Outline platelets.
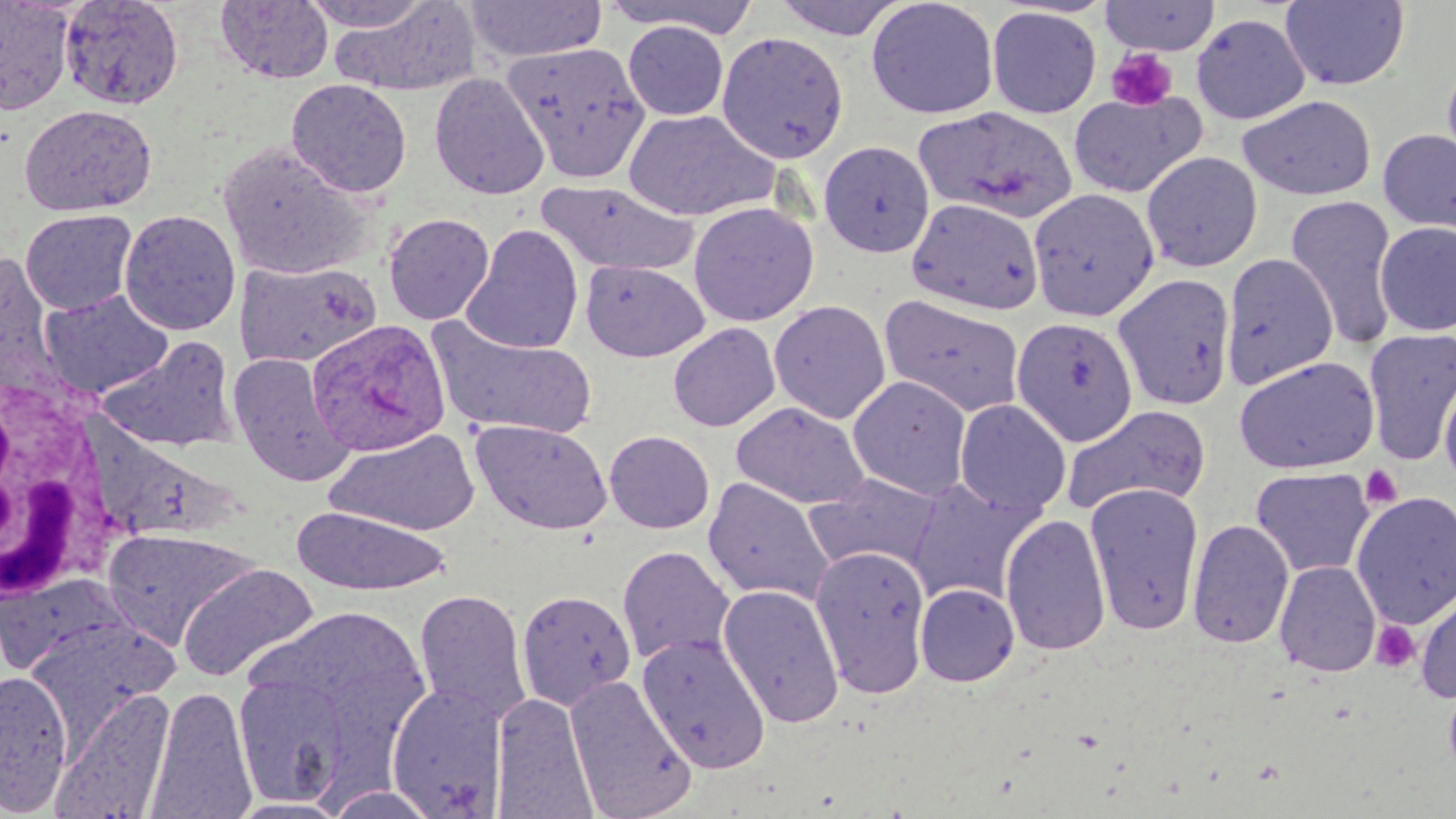
Approximate bounding boxes as named x1/y1/x2/y2 corners in pixels.
Platelets: (x1=1106, y1=48, x2=1179, y2=112), (x1=1360, y1=465, x2=1403, y2=508), (x1=1370, y1=620, x2=1420, y2=672).

Summary:
  - Plasmodium ovale-infected red blood cell locations: (x1=306, y1=319, x2=451, y2=456)
  - White blood cell locations: (x1=0, y1=368, x2=113, y2=607)
  - Uninfected red blood cell locations: (x1=0, y1=0, x2=75, y2=115), (x1=59, y1=0, x2=184, y2=110), (x1=300, y1=0, x2=435, y2=31), (x1=465, y1=0, x2=607, y2=63), (x1=771, y1=0, x2=911, y2=41), (x1=865, y1=0, x2=999, y2=119), (x1=215, y1=1, x2=334, y2=85), (x1=599, y1=1, x2=762, y2=38), (x1=1098, y1=1, x2=1222, y2=55), (x1=1279, y1=1, x2=1409, y2=90), (x1=332, y1=2, x2=480, y2=97), (x1=986, y1=6, x2=1102, y2=119), (x1=1191, y1=14, x2=1310, y2=124), (x1=623, y1=20, x2=729, y2=121), (x1=716, y1=30, x2=849, y2=164), (x1=504, y1=41, x2=650, y2=180), (x1=1440, y1=59, x2=1456, y2=184), (x1=429, y1=72, x2=550, y2=200), (x1=286, y1=78, x2=412, y2=197), (x1=1068, y1=90, x2=1207, y2=199), (x1=1237, y1=95, x2=1376, y2=201), (x1=19, y1=104, x2=157, y2=216), (x1=915, y1=105, x2=1078, y2=224), (x1=624, y1=109, x2=779, y2=222), (x1=1378, y1=127, x2=1456, y2=236), (x1=818, y1=140, x2=935, y2=257), (x1=217, y1=142, x2=373, y2=280), (x1=1141, y1=151, x2=1263, y2=272), (x1=538, y1=179, x2=696, y2=277), (x1=1028, y1=188, x2=1159, y2=321), (x1=1285, y1=195, x2=1399, y2=351), (x1=906, y1=197, x2=1044, y2=315), (x1=688, y1=202, x2=819, y2=326), (x1=20, y1=208, x2=138, y2=314), (x1=119, y1=209, x2=241, y2=335), (x1=383, y1=212, x2=495, y2=325), (x1=1374, y1=222, x2=1456, y2=337), (x1=461, y1=224, x2=584, y2=355), (x1=1220, y1=253, x2=1338, y2=390), (x1=0, y1=254, x2=59, y2=388), (x1=235, y1=259, x2=382, y2=368), (x1=581, y1=260, x2=710, y2=362), (x1=1112, y1=273, x2=1237, y2=410), (x1=39, y1=289, x2=174, y2=398), (x1=879, y1=294, x2=1026, y2=418), (x1=769, y1=299, x2=891, y2=424), (x1=428, y1=317, x2=597, y2=440), (x1=1011, y1=317, x2=1139, y2=446), (x1=667, y1=322, x2=781, y2=432), (x1=1363, y1=328, x2=1456, y2=465), (x1=96, y1=336, x2=240, y2=452), (x1=228, y1=353, x2=354, y2=486), (x1=1233, y1=355, x2=1380, y2=474), (x1=1439, y1=371, x2=1456, y2=493), (x1=848, y1=375, x2=972, y2=499), (x1=954, y1=399, x2=1071, y2=517), (x1=731, y1=402, x2=870, y2=510), (x1=1061, y1=403, x2=1213, y2=519), (x1=470, y1=419, x2=612, y2=535), (x1=326, y1=427, x2=481, y2=536), (x1=604, y1=430, x2=715, y2=534), (x1=1251, y1=467, x2=1375, y2=578), (x1=805, y1=472, x2=944, y2=574), (x1=905, y1=476, x2=1044, y2=607), (x1=702, y1=477, x2=834, y2=605), (x1=1084, y1=482, x2=1204, y2=635), (x1=1351, y1=491, x2=1456, y2=629), (x1=291, y1=506, x2=450, y2=596), (x1=1000, y1=513, x2=1111, y2=656), (x1=1187, y1=518, x2=1294, y2=649), (x1=102, y1=527, x2=258, y2=650), (x1=616, y1=545, x2=735, y2=666), (x1=810, y1=545, x2=932, y2=698), (x1=1274, y1=560, x2=1381, y2=677), (x1=177, y1=563, x2=319, y2=684), (x1=0, y1=573, x2=138, y2=677), (x1=717, y1=583, x2=845, y2=729), (x1=915, y1=583, x2=1020, y2=686), (x1=1415, y1=587, x2=1456, y2=702), (x1=413, y1=588, x2=532, y2=725), (x1=517, y1=589, x2=636, y2=711), (x1=238, y1=605, x2=433, y2=780), (x1=25, y1=616, x2=178, y2=744), (x1=636, y1=632, x2=772, y2=775), (x1=0, y1=670, x2=74, y2=814), (x1=233, y1=672, x2=354, y2=807), (x1=564, y1=674, x2=697, y2=819), (x1=386, y1=683, x2=509, y2=818), (x1=148, y1=685, x2=256, y2=817), (x1=51, y1=688, x2=175, y2=819), (x1=492, y1=692, x2=596, y2=816), (x1=319, y1=786, x2=444, y2=818), (x1=226, y1=797, x2=353, y2=818)
  - Slide-level diagnosis: Plasmodium ovale
  - Stain: May-Grünwald-Giemsa
  - Magnification: 1000x
  - Field of view: single
  - Preparation: thin blood smear
  - Modality: optical microscopy
  - Image size: 1456×819 pixels